Identify the parasite.
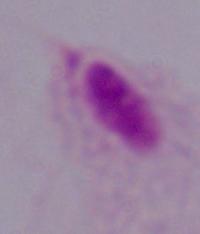

A trichomonad.

Summary:
  - Modality: photomicrograph
  - Magnification: 1000x